Identify the cell.
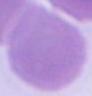
An erythrocyte.

Summary:
  - Modality: photomicrograph
  - Magnification: 1000x